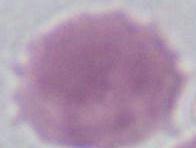

Summary:
  - Modality: photomicrograph
  - Magnification: 1000x
  - Identification: red blood cell